Give the position of every Plasmodium parasite visible.
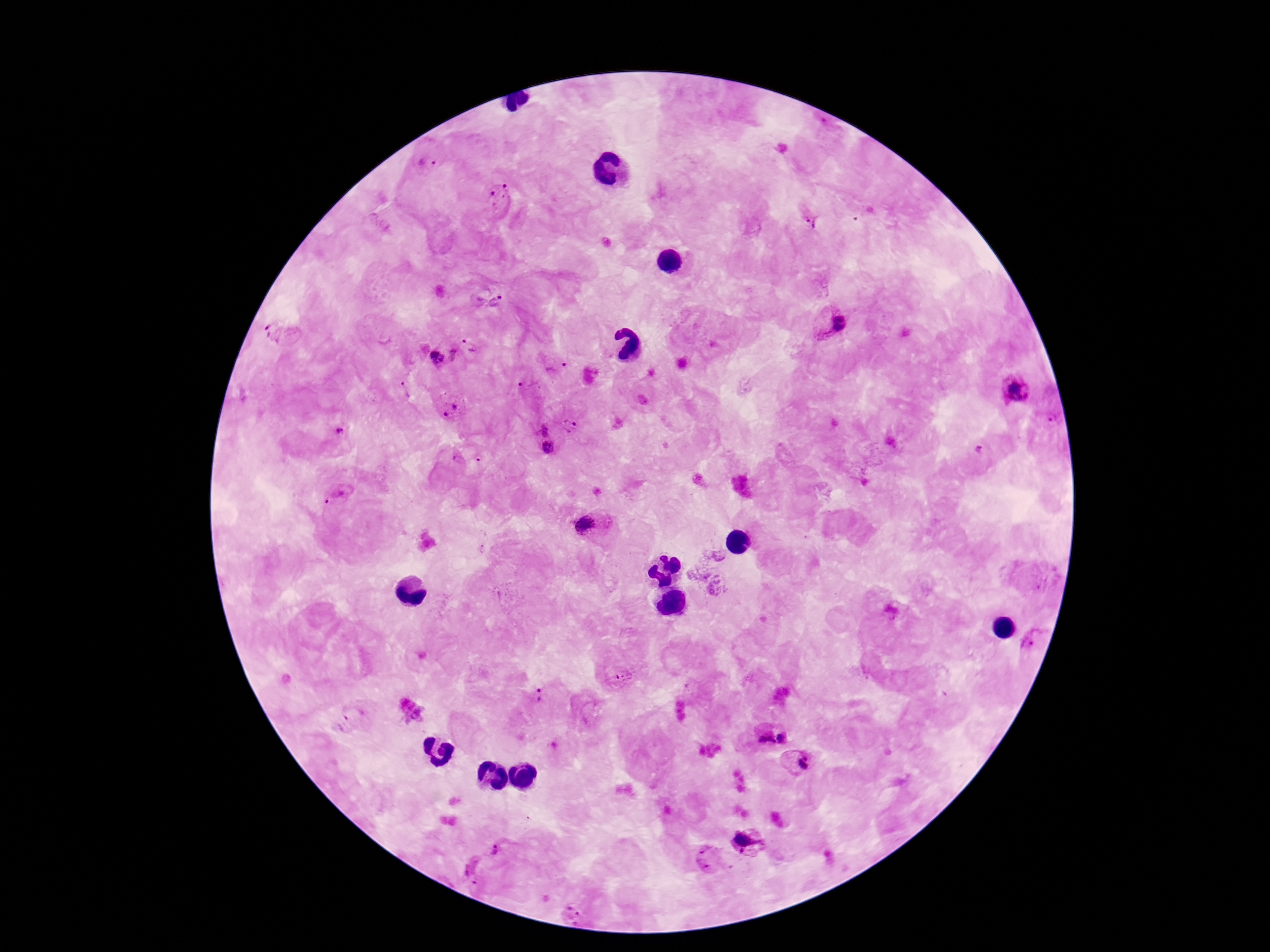

Approximate centers as [x, y] in pixels.
Plasmodium parasites: [428, 164], [499, 198], [809, 219], [492, 302], [830, 324], [277, 332], [470, 341], [457, 355], [434, 357], [557, 367], [529, 385], [1015, 388], [405, 389], [451, 407], [1050, 419], [618, 424], [571, 426], [336, 429], [541, 429], [548, 448], [979, 450], [459, 459], [334, 496], [591, 526], [718, 557], [699, 573], [717, 586], [1035, 638], [625, 677], [539, 696], [340, 723], [783, 737], [763, 738], [799, 763], [750, 840], [501, 850], [713, 859], [475, 869], [571, 911].

{
  "capture": "smartphone camera through the microscope eyepiece",
  "stain": "Giemsa",
  "magnification": "100x",
  "image_size": "1270×952 pixels",
  "field_of_view": "single",
  "patient_malaria_status": "infected",
  "preparation": "thick blood film"
}